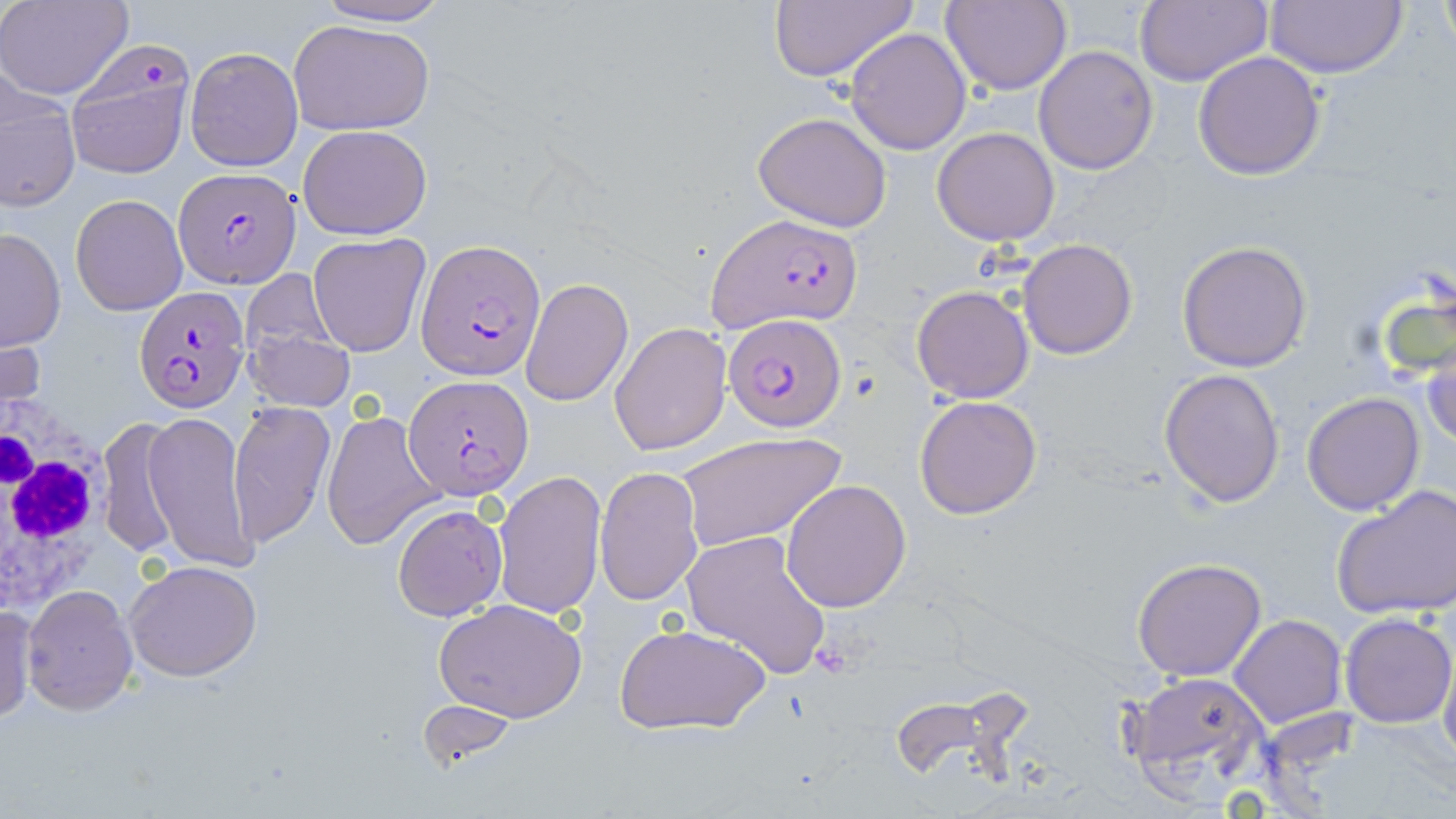
slide-level diagnosis = Plasmodium falciparum
image size = 1456×819 pixels
preparation = thin blood film
Plasmodium falciparum-infected red blood cell locations = approximate bounding boxes as named x1/y1/x2/y2 corners in pixels: (x1=174, y1=167, x2=299, y2=287), (x1=707, y1=213, x2=862, y2=333), (x1=418, y1=240, x2=546, y2=378), (x1=135, y1=287, x2=252, y2=412), (x1=723, y1=314, x2=847, y2=432), (x1=403, y1=375, x2=531, y2=500)
field of view = one of a larger specimen
uninfected red blood cell locations = approximate bounding boxes as named x1/y1/x2/y2 corners in pixels: (x1=311, y1=0, x2=454, y2=28), (x1=767, y1=0, x2=916, y2=86), (x1=941, y1=0, x2=1073, y2=95), (x1=1134, y1=0, x2=1272, y2=87), (x1=1264, y1=0, x2=1409, y2=79), (x1=1437, y1=0, x2=1454, y2=56), (x1=0, y1=1, x2=134, y2=100), (x1=287, y1=18, x2=435, y2=135), (x1=844, y1=27, x2=971, y2=155), (x1=63, y1=41, x2=197, y2=179), (x1=1033, y1=44, x2=1160, y2=176), (x1=184, y1=46, x2=303, y2=171), (x1=1192, y1=49, x2=1326, y2=179), (x1=0, y1=71, x2=80, y2=212), (x1=753, y1=111, x2=894, y2=232), (x1=297, y1=124, x2=432, y2=238), (x1=931, y1=127, x2=1059, y2=246), (x1=71, y1=194, x2=188, y2=316), (x1=0, y1=228, x2=66, y2=352), (x1=307, y1=232, x2=431, y2=357), (x1=1017, y1=238, x2=1138, y2=359), (x1=1175, y1=240, x2=1313, y2=372), (x1=239, y1=269, x2=346, y2=382), (x1=521, y1=278, x2=633, y2=406), (x1=911, y1=285, x2=1035, y2=403), (x1=1, y1=309, x2=50, y2=421), (x1=243, y1=313, x2=357, y2=414), (x1=609, y1=322, x2=733, y2=456), (x1=1421, y1=335, x2=1456, y2=452), (x1=1159, y1=368, x2=1287, y2=508), (x1=1301, y1=392, x2=1426, y2=514), (x1=913, y1=394, x2=1043, y2=520), (x1=228, y1=402, x2=335, y2=549), (x1=322, y1=409, x2=444, y2=549), (x1=143, y1=411, x2=257, y2=572), (x1=98, y1=416, x2=183, y2=561), (x1=676, y1=433, x2=844, y2=550), (x1=595, y1=468, x2=704, y2=605), (x1=493, y1=470, x2=607, y2=621), (x1=781, y1=479, x2=912, y2=613), (x1=1332, y1=482, x2=1456, y2=619), (x1=393, y1=503, x2=507, y2=622), (x1=682, y1=529, x2=832, y2=679), (x1=1132, y1=558, x2=1268, y2=681), (x1=124, y1=560, x2=263, y2=682), (x1=22, y1=584, x2=137, y2=716), (x1=433, y1=597, x2=588, y2=722), (x1=1, y1=600, x2=38, y2=724), (x1=1339, y1=612, x2=1455, y2=729), (x1=1229, y1=614, x2=1346, y2=727), (x1=615, y1=619, x2=772, y2=736), (x1=1440, y1=650, x2=1456, y2=772), (x1=1120, y1=671, x2=1273, y2=803), (x1=413, y1=700, x2=525, y2=772)
modality = optical microscopy
magnification = 1000x
white blood cell locations = approximate bounding boxes as named x1/y1/x2/y2 corners in pixels: (x1=0, y1=418, x2=110, y2=607)
stain = May-Grünwald-Giemsa